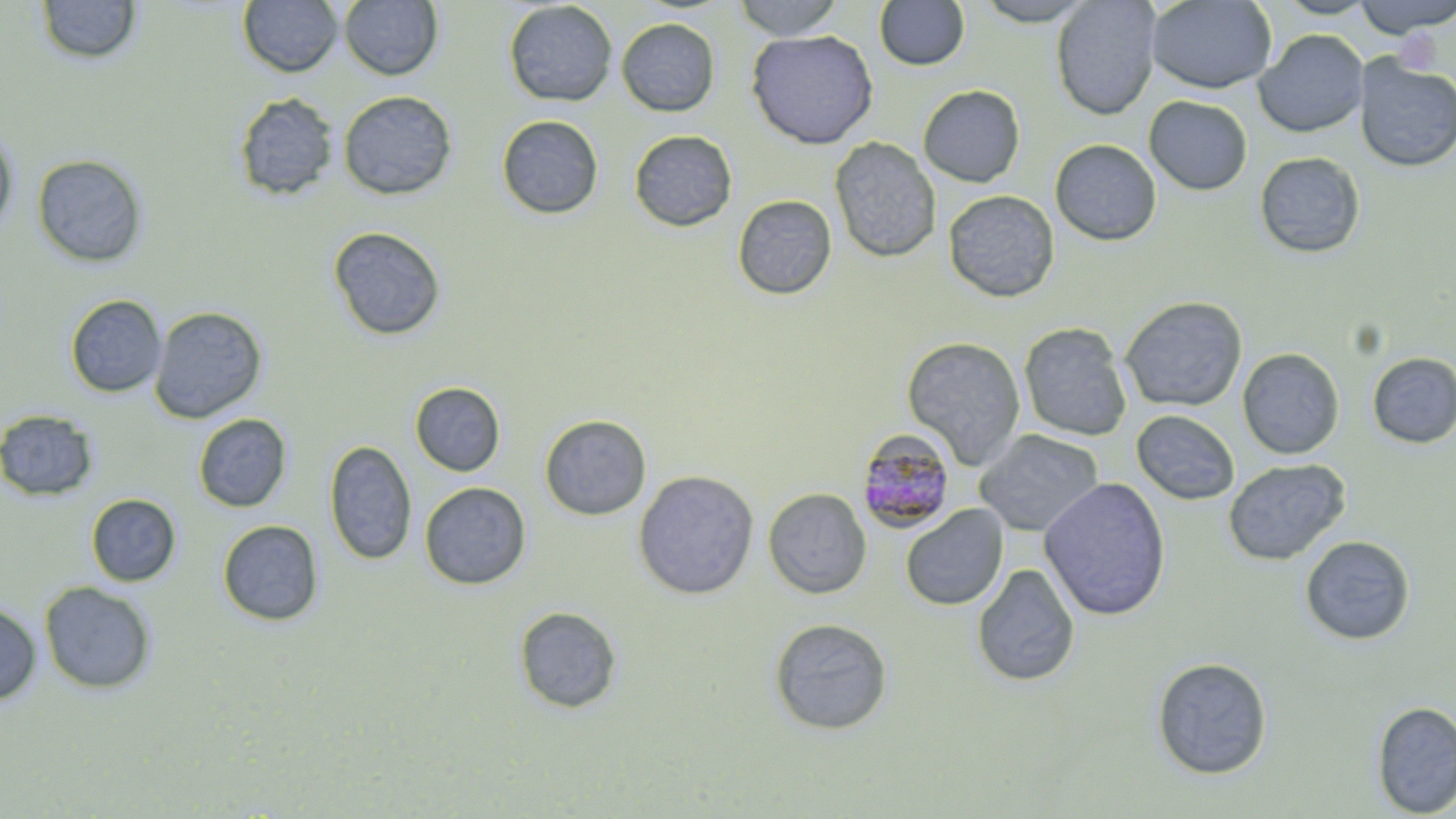
slide-level diagnosis = Plasmodium malariae
uninfected red blood cell locations = approximate bounding boxes as named x1/y1/x2/y2 corners in pixels: (x1=36, y1=0, x2=143, y2=66), (x1=733, y1=0, x2=843, y2=40), (x1=972, y1=0, x2=1096, y2=26), (x1=1050, y1=0, x2=1161, y2=120), (x1=1147, y1=0, x2=1276, y2=94), (x1=1273, y1=0, x2=1378, y2=19), (x1=1352, y1=0, x2=1456, y2=37), (x1=238, y1=1, x2=344, y2=77), (x1=339, y1=1, x2=443, y2=81), (x1=503, y1=1, x2=618, y2=107), (x1=874, y1=1, x2=970, y2=71), (x1=616, y1=17, x2=721, y2=117), (x1=746, y1=29, x2=879, y2=150), (x1=1253, y1=29, x2=1369, y2=138), (x1=1354, y1=55, x2=1456, y2=172), (x1=918, y1=84, x2=1025, y2=188), (x1=338, y1=90, x2=457, y2=200), (x1=233, y1=92, x2=340, y2=201), (x1=1144, y1=96, x2=1252, y2=195), (x1=496, y1=115, x2=604, y2=220), (x1=0, y1=124, x2=19, y2=237), (x1=629, y1=129, x2=738, y2=232), (x1=829, y1=136, x2=942, y2=263), (x1=1049, y1=139, x2=1162, y2=246), (x1=1254, y1=151, x2=1366, y2=259), (x1=32, y1=153, x2=149, y2=269), (x1=943, y1=190, x2=1060, y2=303), (x1=732, y1=194, x2=837, y2=300), (x1=327, y1=226, x2=446, y2=341), (x1=64, y1=294, x2=167, y2=398), (x1=1119, y1=295, x2=1248, y2=413), (x1=149, y1=306, x2=268, y2=424), (x1=1018, y1=322, x2=1132, y2=442), (x1=902, y1=335, x2=1026, y2=469), (x1=1237, y1=347, x2=1345, y2=460), (x1=1366, y1=352, x2=1456, y2=449), (x1=410, y1=382, x2=506, y2=477), (x1=0, y1=409, x2=99, y2=502), (x1=1130, y1=410, x2=1240, y2=506), (x1=193, y1=413, x2=292, y2=513), (x1=538, y1=414, x2=652, y2=521), (x1=974, y1=429, x2=1105, y2=537), (x1=324, y1=439, x2=417, y2=567), (x1=1222, y1=458, x2=1350, y2=566), (x1=633, y1=470, x2=759, y2=600), (x1=1038, y1=477, x2=1172, y2=620), (x1=420, y1=481, x2=531, y2=590), (x1=763, y1=487, x2=872, y2=599), (x1=86, y1=493, x2=181, y2=586), (x1=900, y1=503, x2=1008, y2=611), (x1=217, y1=519, x2=324, y2=626), (x1=1299, y1=535, x2=1415, y2=645), (x1=971, y1=562, x2=1080, y2=687), (x1=38, y1=581, x2=157, y2=694), (x1=0, y1=601, x2=42, y2=706), (x1=514, y1=605, x2=622, y2=714), (x1=768, y1=617, x2=893, y2=736), (x1=1151, y1=656, x2=1273, y2=780), (x1=1371, y1=700, x2=1456, y2=817)
Plasmodium malariae-infected red blood cell locations = approximate bounding boxes as named x1/y1/x2/y2 corners in pixels: (x1=855, y1=428, x2=958, y2=534)
preparation = thin blood film
stain = May-Grünwald-Giemsa
field of view = one of a larger specimen
image size = 1456×819 pixels
magnification = 1000x
modality = optical microscopy